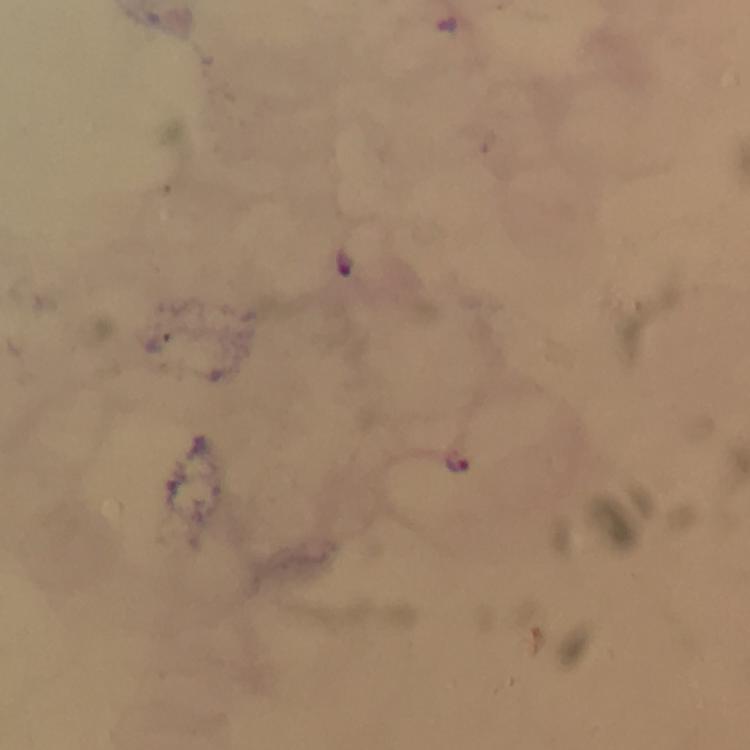

Approximate centers as [x, y] in pixels.
Summary:
  - Plasmodium parasite locations: [448, 22], [346, 263], [458, 462]
  - Stain: Giemsa
  - Immersion oil: applied
  - Context: from a malaria diagnostic workup
  - Magnification: 100x
  - Capture: smartphone mounted on the microscope
  - Preparation: thick smear
  - Image size: 750×750 pixels
  - Cropped from: one field of view